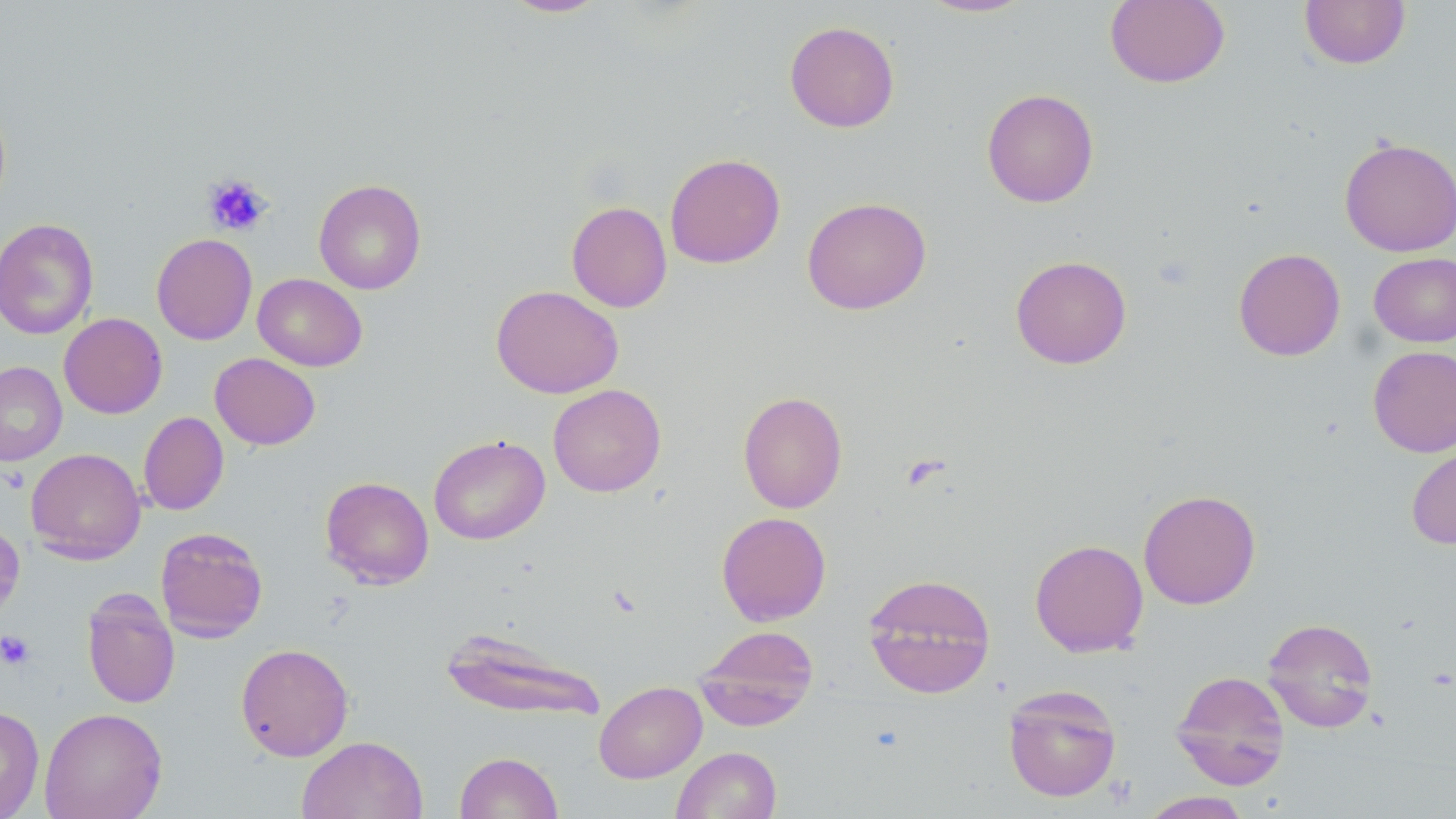

slide-level diagnosis = no evidence of blood parasites
magnification = 1000x
field of view = single
modality = optical microscopy
preparation = thin blood film
image size = 1456×819 pixels
stain = May-Grünwald-Giemsa
platelet locations = approximate bounding boxes as named x1/y1/x2/y2 corners in pixels: (x1=203, y1=174, x2=271, y2=236), (x1=0, y1=630, x2=35, y2=670)
uninfected red blood cell locations = approximate bounding boxes as named x1/y1/x2/y2 corners in pixels: (x1=499, y1=0, x2=611, y2=18), (x1=918, y1=0, x2=1033, y2=17), (x1=1105, y1=0, x2=1230, y2=88), (x1=1299, y1=0, x2=1411, y2=69), (x1=784, y1=21, x2=900, y2=133), (x1=981, y1=88, x2=1099, y2=207), (x1=1339, y1=137, x2=1456, y2=256), (x1=665, y1=153, x2=785, y2=269), (x1=313, y1=178, x2=427, y2=295), (x1=802, y1=196, x2=932, y2=315), (x1=566, y1=201, x2=672, y2=312), (x1=0, y1=218, x2=100, y2=340), (x1=151, y1=233, x2=258, y2=345), (x1=1233, y1=248, x2=1345, y2=361), (x1=1369, y1=252, x2=1456, y2=347), (x1=1010, y1=255, x2=1132, y2=369), (x1=252, y1=273, x2=367, y2=371), (x1=491, y1=284, x2=624, y2=399), (x1=59, y1=313, x2=167, y2=419), (x1=1368, y1=345, x2=1456, y2=458), (x1=209, y1=353, x2=321, y2=450), (x1=0, y1=361, x2=67, y2=466), (x1=548, y1=384, x2=666, y2=498), (x1=737, y1=390, x2=848, y2=514), (x1=139, y1=412, x2=229, y2=515), (x1=428, y1=434, x2=550, y2=545), (x1=1406, y1=439, x2=1456, y2=550), (x1=26, y1=447, x2=146, y2=564), (x1=320, y1=476, x2=434, y2=589), (x1=1138, y1=489, x2=1261, y2=609), (x1=716, y1=511, x2=831, y2=626), (x1=0, y1=517, x2=25, y2=625), (x1=155, y1=527, x2=268, y2=643), (x1=1029, y1=539, x2=1148, y2=657), (x1=863, y1=572, x2=996, y2=698), (x1=81, y1=588, x2=180, y2=708), (x1=1261, y1=617, x2=1379, y2=732), (x1=694, y1=624, x2=820, y2=730), (x1=439, y1=626, x2=606, y2=723), (x1=235, y1=643, x2=354, y2=761), (x1=1171, y1=670, x2=1290, y2=789), (x1=594, y1=681, x2=707, y2=783), (x1=1003, y1=684, x2=1122, y2=802), (x1=0, y1=705, x2=45, y2=819), (x1=40, y1=707, x2=167, y2=819), (x1=296, y1=735, x2=428, y2=819), (x1=671, y1=746, x2=781, y2=818), (x1=454, y1=751, x2=564, y2=819), (x1=1139, y1=791, x2=1253, y2=819)